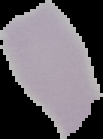

Summary:
  - Malaria status: uninfected
  - Image size: 103×139 pixels
  - Image type: segmented cell region with the area outside set to black
  - Preparation: thin blood smear